Comment on the morphology of the red blood cells.
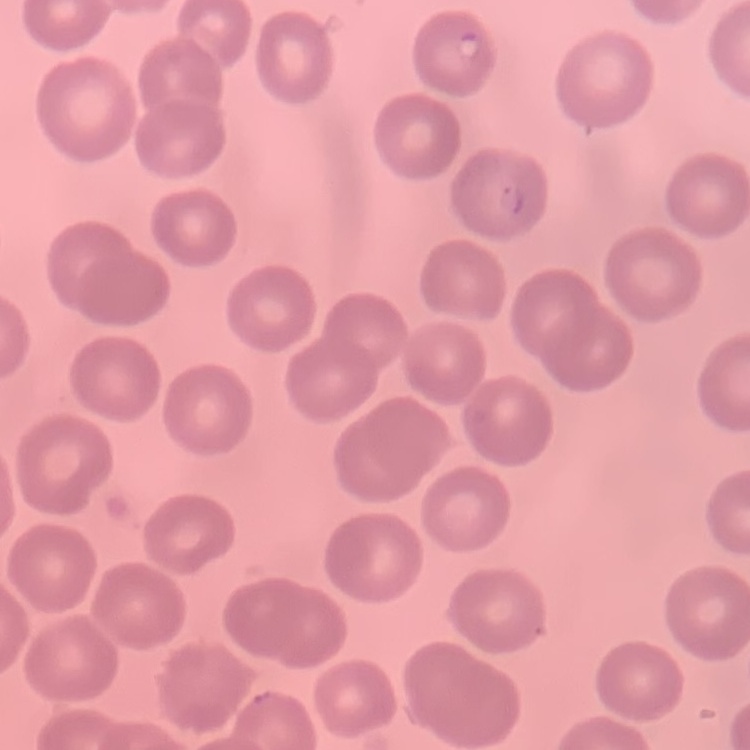
No rouleaux formation.

preparation: thin blood smear
image_type: one tile cut from a larger photomicrograph
stain: Field's or Giemsa